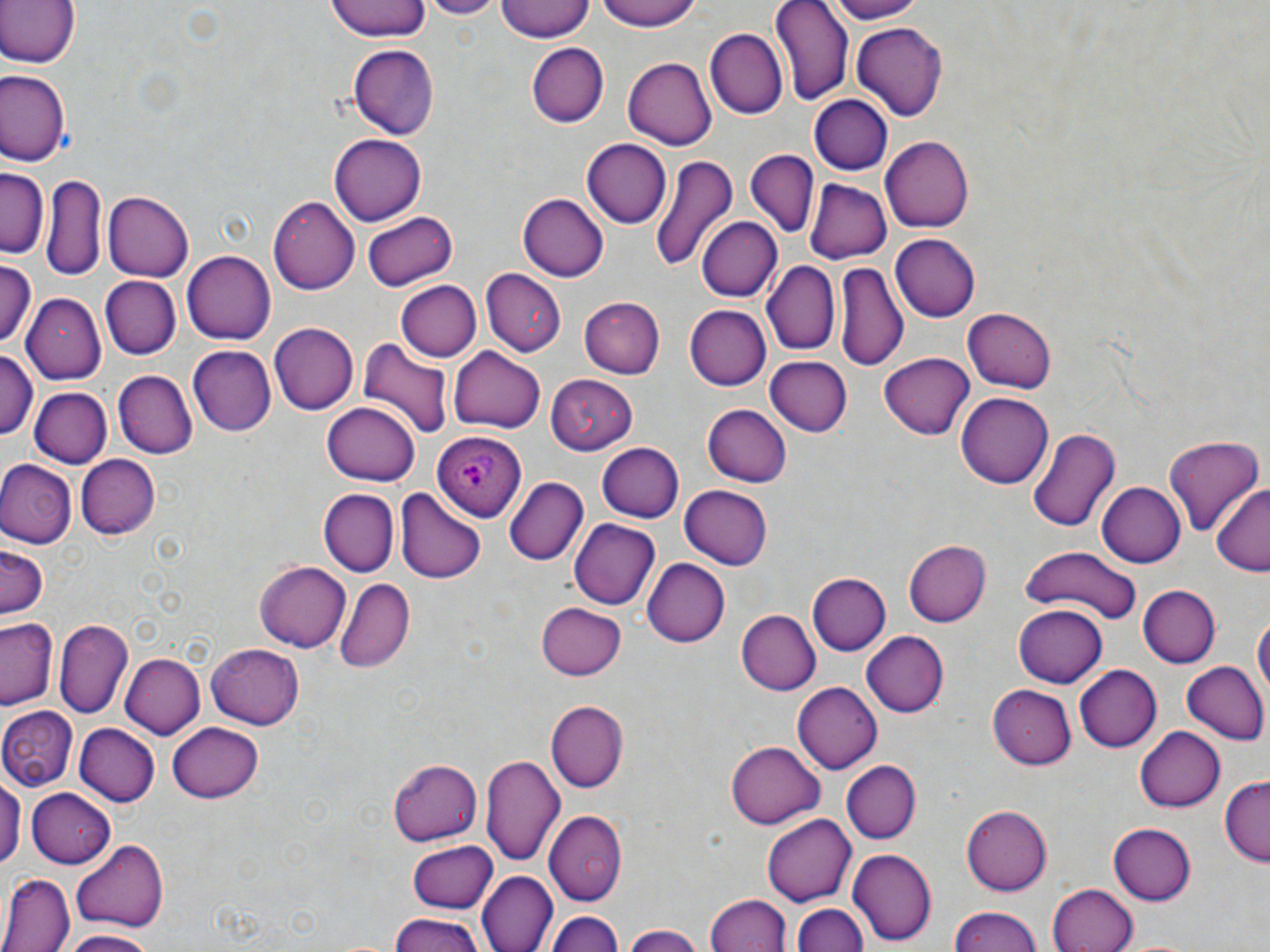
Approximate bounding boxes as (x1, y1, x2, y2) in pixels. Plasmodium ovale-infected red blood cell locations: (434, 428, 526, 523). Uninfected red blood cell locations: (0, 0, 80, 69), (324, 0, 434, 42), (422, 0, 499, 18), (497, 0, 595, 42), (593, 0, 707, 31), (770, 0, 853, 106), (823, 0, 924, 24), (851, 22, 948, 117), (707, 28, 788, 118), (526, 42, 608, 129), (347, 44, 439, 140), (624, 56, 716, 150), (0, 69, 70, 168), (808, 95, 892, 175), (328, 134, 427, 226), (881, 135, 973, 233), (583, 138, 671, 228), (745, 148, 817, 238), (650, 154, 741, 272), (0, 170, 47, 256), (42, 172, 106, 280), (803, 177, 891, 262), (103, 189, 193, 280), (518, 191, 608, 279), (267, 195, 359, 294), (362, 211, 457, 290), (696, 216, 781, 302), (891, 233, 979, 323), (182, 250, 275, 345), (0, 260, 37, 348), (762, 261, 840, 355), (834, 262, 907, 370), (479, 267, 566, 355), (100, 276, 181, 360), (396, 281, 480, 362), (24, 294, 106, 386), (582, 297, 665, 378), (683, 303, 771, 390), (571, 305, 753, 381), (963, 307, 1057, 393), (269, 322, 359, 416), (359, 339, 452, 442), (185, 345, 276, 437), (449, 345, 545, 435), (0, 347, 38, 445), (881, 350, 974, 436), (765, 358, 852, 436), (113, 369, 197, 461), (545, 373, 637, 453), (28, 385, 111, 466), (958, 393, 1053, 489), (323, 400, 421, 484), (702, 404, 793, 487), (1028, 426, 1121, 534), (1163, 435, 1264, 535), (597, 442, 684, 521), (75, 453, 161, 540), (0, 459, 76, 548), (504, 477, 588, 566), (1098, 482, 1184, 567), (680, 485, 772, 570), (1210, 485, 1270, 576), (393, 487, 487, 584), (317, 488, 398, 576), (570, 518, 659, 609), (902, 540, 990, 628), (1, 546, 46, 618), (1020, 548, 1142, 626), (643, 559, 730, 647), (255, 562, 350, 652), (806, 572, 891, 657), (334, 577, 415, 673), (1138, 584, 1220, 669), (536, 602, 626, 679), (1013, 605, 1107, 689), (736, 610, 819, 694), (1250, 610, 1269, 710), (2, 616, 60, 711), (56, 620, 131, 718), (863, 631, 948, 718), (205, 643, 306, 729), (120, 653, 205, 739), (1182, 661, 1268, 744), (1074, 664, 1162, 752), (791, 682, 880, 774), (989, 686, 1078, 767), (546, 700, 627, 793), (0, 706, 77, 790), (168, 720, 263, 801), (75, 724, 159, 805), (1135, 725, 1226, 812), (727, 738, 826, 829), (481, 753, 564, 866), (388, 759, 482, 845), (840, 760, 921, 844), (0, 771, 22, 875), (1218, 779, 1270, 866), (26, 790, 115, 866), (960, 804, 1051, 896), (545, 811, 627, 905), (762, 813, 857, 905), (1108, 822, 1196, 903), (72, 839, 169, 930), (407, 840, 498, 913), (848, 848, 938, 944), (479, 871, 555, 952), (1, 872, 73, 952), (1049, 883, 1139, 952), (707, 894, 791, 951), (790, 900, 870, 952), (944, 905, 1046, 952), (546, 911, 625, 952), (385, 915, 485, 951), (621, 924, 704, 952), (61, 930, 157, 952). Slide-level diagnosis: Plasmodium ovale. Optical microscopy. May-Grünwald-Giemsa-stained preparation. Captured at 1000x magnification. Single field of view. Image is 1270×952 pixels. Thin blood smear.